State which parasite is depicted.
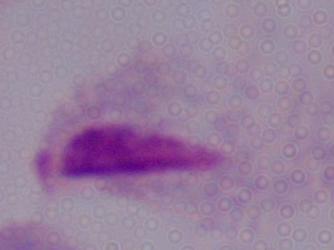

This is a trichomonad.

{
  "modality": "photomicrograph",
  "magnification": "1000x"
}